State which parasite is depicted.
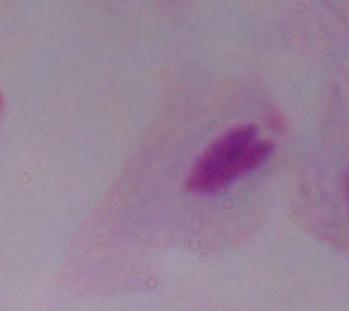

This is a trichomonad.

magnification = 1000x
modality = micrograph